Outline each uninfected red blood cell.
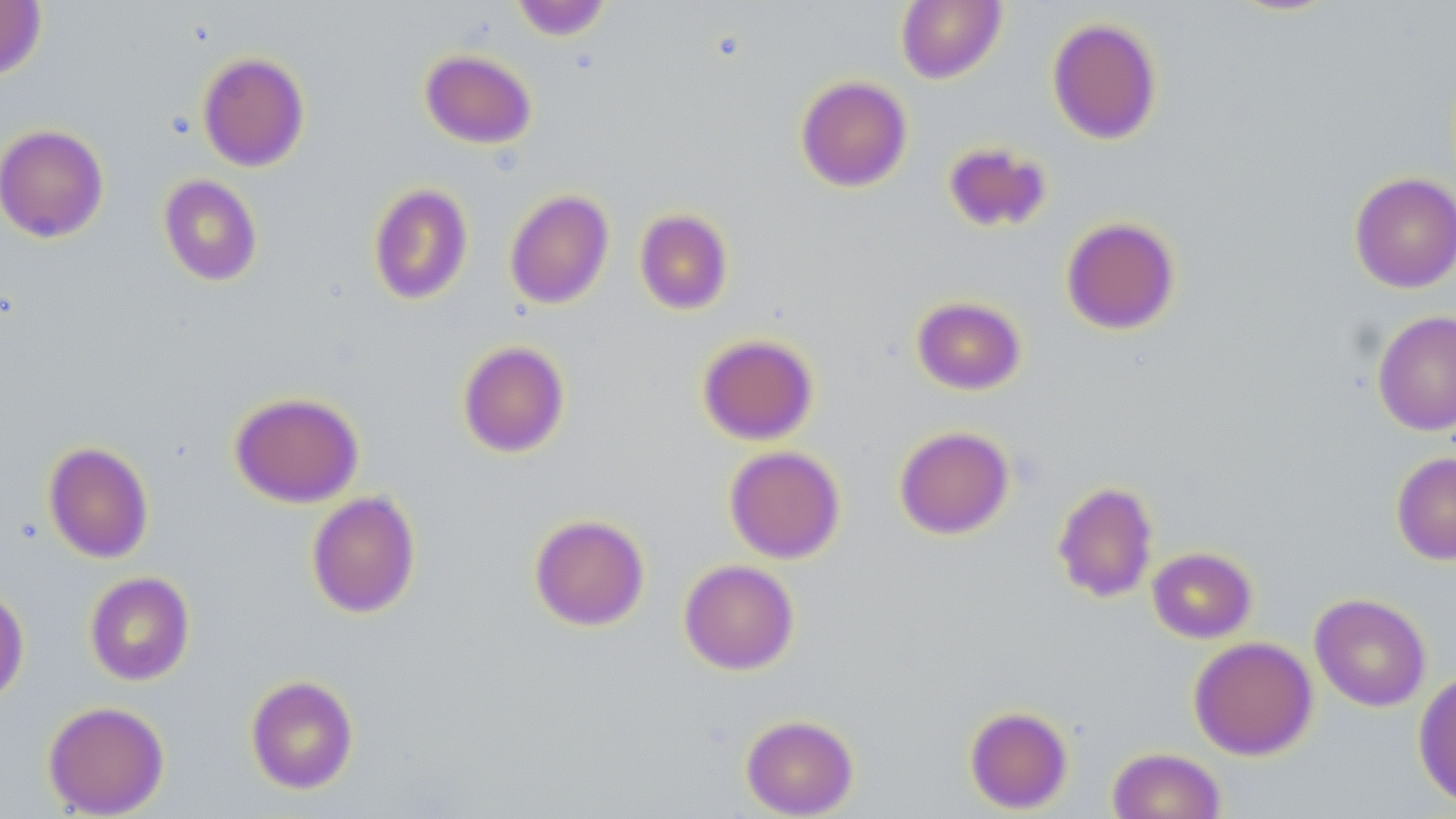
Approximate bounding boxes as (x1,y1)-(x2,y2) corner pairs in pixels.
Uninfected red blood cells: (509,0)-(612,41), (896,0)-(1006,84), (0,1)-(47,81), (1047,17)-(1163,145), (420,49)-(536,149), (197,51)-(310,172), (795,75)-(913,192), (0,124)-(109,243), (942,141)-(1053,233), (1349,172)-(1456,293), (158,175)-(263,286), (368,183)-(474,305), (504,189)-(614,310), (634,208)-(734,315), (1061,216)-(1181,335), (911,295)-(1027,395), (1372,310)-(1456,436), (697,333)-(819,445), (457,340)-(570,457), (229,391)-(364,508), (893,425)-(1014,540), (42,441)-(154,564), (724,446)-(845,564), (1391,452)-(1456,565), (1052,481)-(1158,602), (306,490)-(420,618), (528,513)-(650,631), (1147,546)-(1257,643), (678,559)-(800,675), (84,571)-(195,686), (0,583)-(30,707), (1309,592)-(1432,712), (1188,636)-(1318,760), (1413,668)-(1456,812), (245,674)-(359,794), (42,701)-(170,817), (964,706)-(1073,814), (740,714)-(859,818), (1107,747)-(1227,819).

{
  "slide_level_diagnosis": "negative for blood parasites",
  "field_of_view": "single",
  "modality": "optical microscopy",
  "preparation": "thin blood film",
  "image_size": "1456×819 pixels",
  "magnification": "1000x",
  "stain": "May-Grünwald-Giemsa"
}